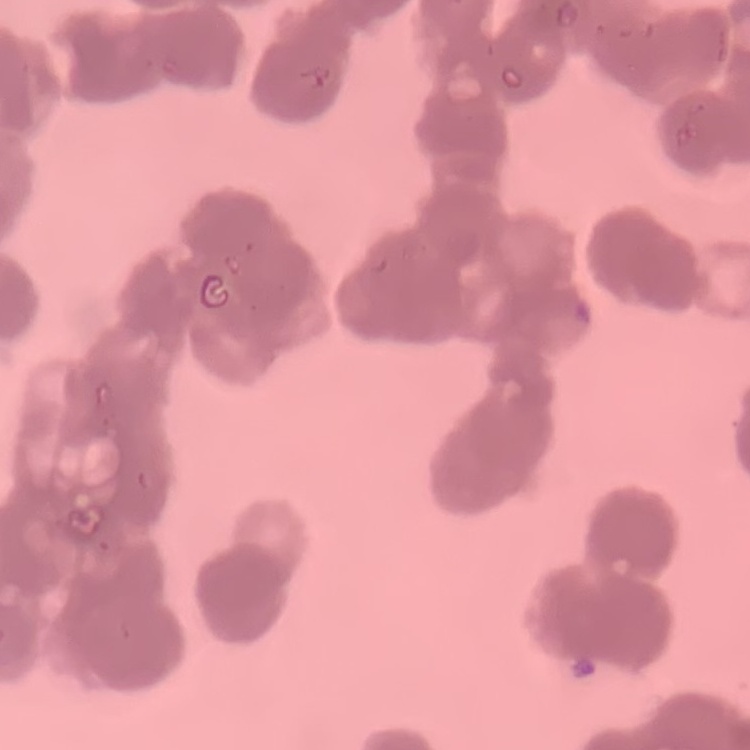
erythrocyte morphology = rouleaux formation
image type = square crop of a larger photomicrograph
stain = Field's or Giemsa
preparation = thin blood smear